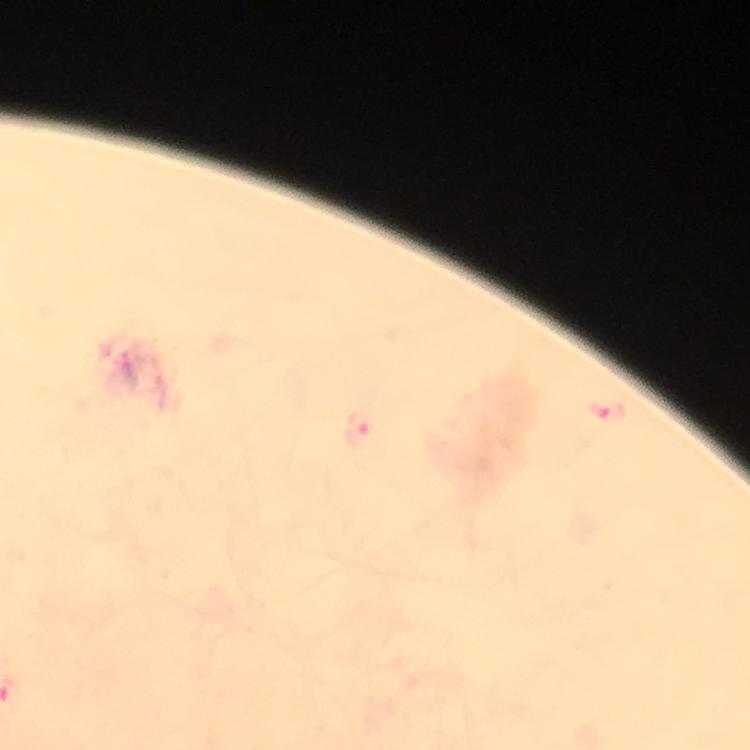

Approximate object centers, in pixels from the top-left corner. Malaria parasite locations: (x=607, y=412), (x=358, y=428). From a diagnostic examination for malaria. A crop from one field of view. Thick blood smear. 100x magnification. Image is 750×750 pixels. Photographed with a smartphone mounted on the microscope. Giemsa stain. Immersion oil applied.